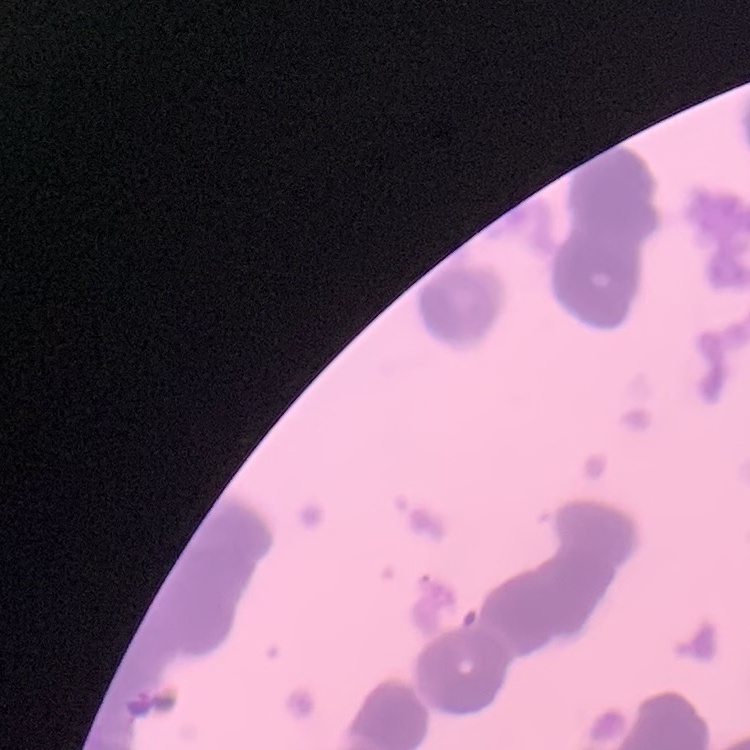

Summary:
  - Erythrocyte morphology: rouleaux formation
  - Stain: Field's or Giemsa
  - Image type: square crop of a larger photomicrograph
  - Preparation: thin blood smear